Name the parasite shown.
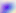

This is Toxoplasma gondii.

Photomicrograph. 400x magnification.